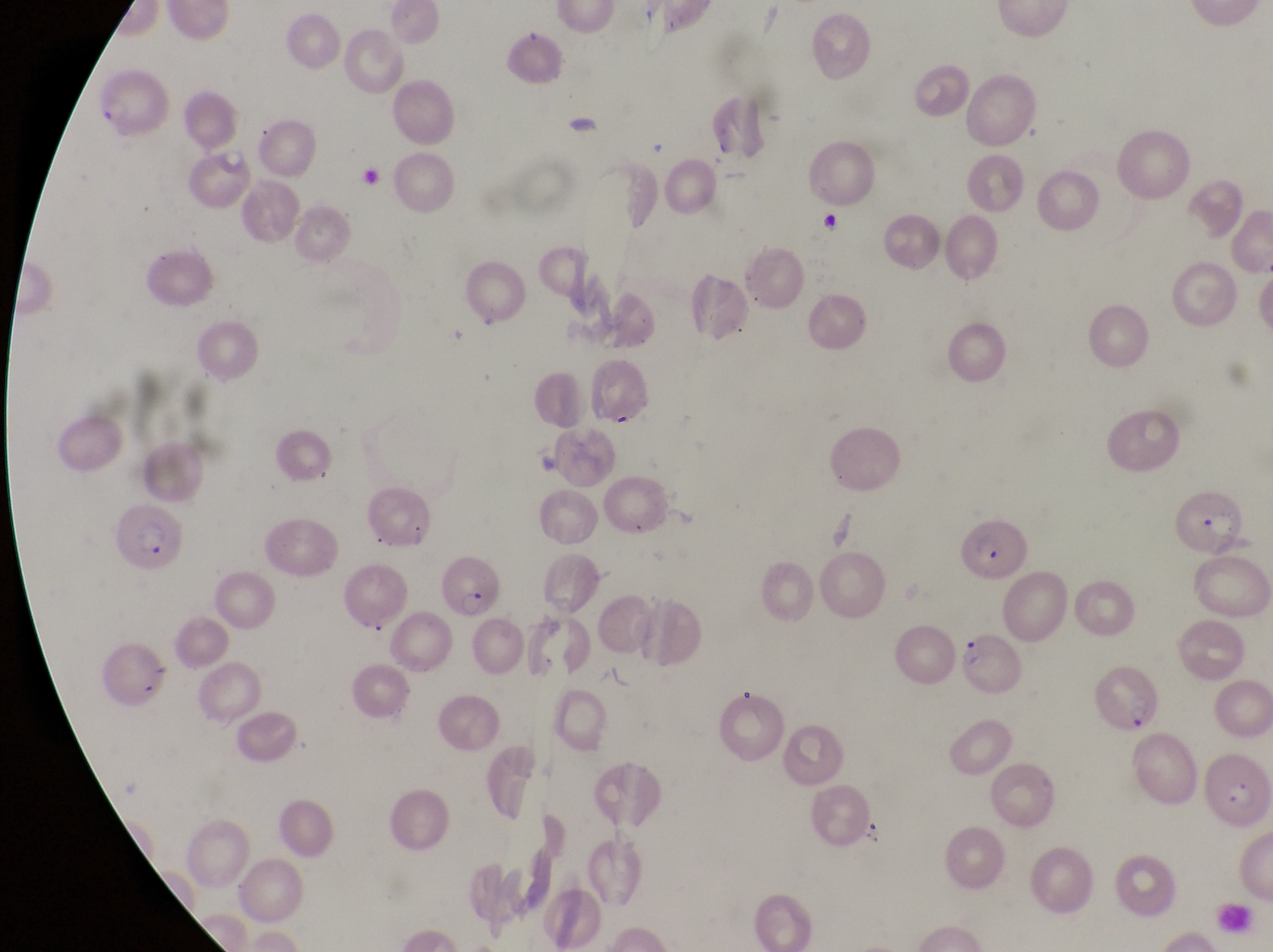

Approximate bounding boxes as left top right bottom in pixels. Parasitised red blood cell locations: 1175 486 1250 548; 117 505 186 579; 958 510 1027 580; 439 552 499 620; 958 631 1027 696; 1203 749 1272 832. Image is 1273×952 pixels. Thin blood smear. At a magnification of 1000x. Captured by a smartphone held over the eyepiece of an Olympus CX-23 microscope. One field of view. Sample from Uganda.